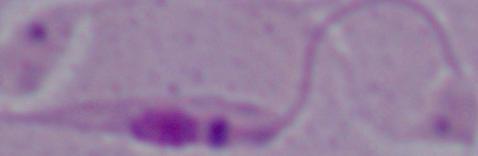
Photomicrograph. Captured at 1000x magnification. A Leishmania parasite is seen.